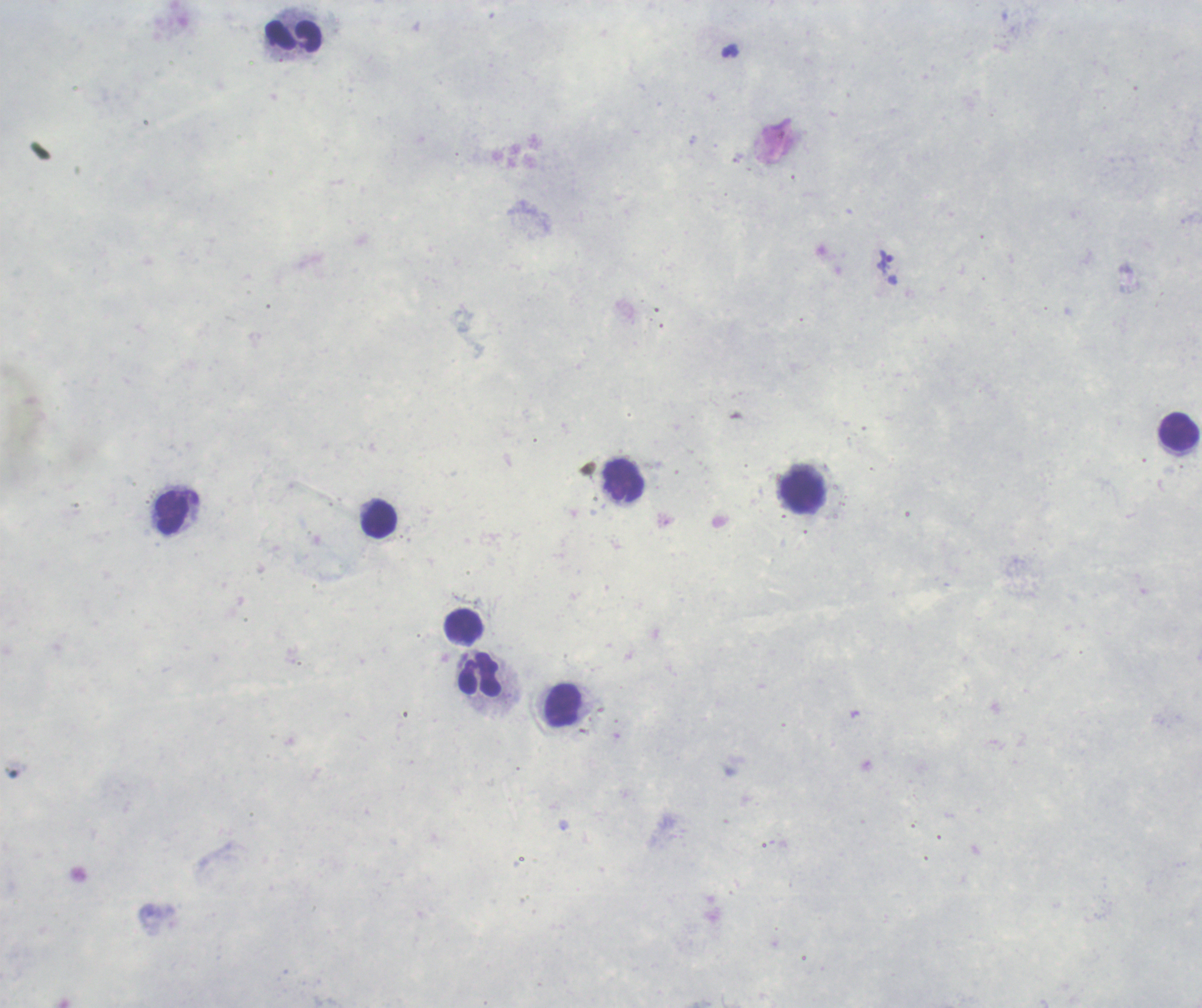

Approximate centers as [x, y] in pixels. Trophozoite locations: [884, 261]. Leukocyte locations: [294, 37], [1180, 432], [624, 481], [803, 492], [172, 514], [380, 520], [464, 627], [479, 673], [564, 704]. Thick blood film. Image is 1202×1008 pixels. Result: positive for Plasmodium parasites. Single field of view. Previously used in an actual diagnosis. Background quality: poor. Romanowsky stain. Captured at 100x magnification.